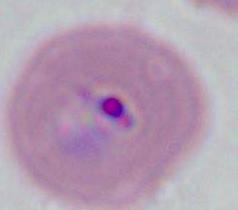

A Plasmodium parasite is shown. 400x or 1000x magnification. Photomicrograph.